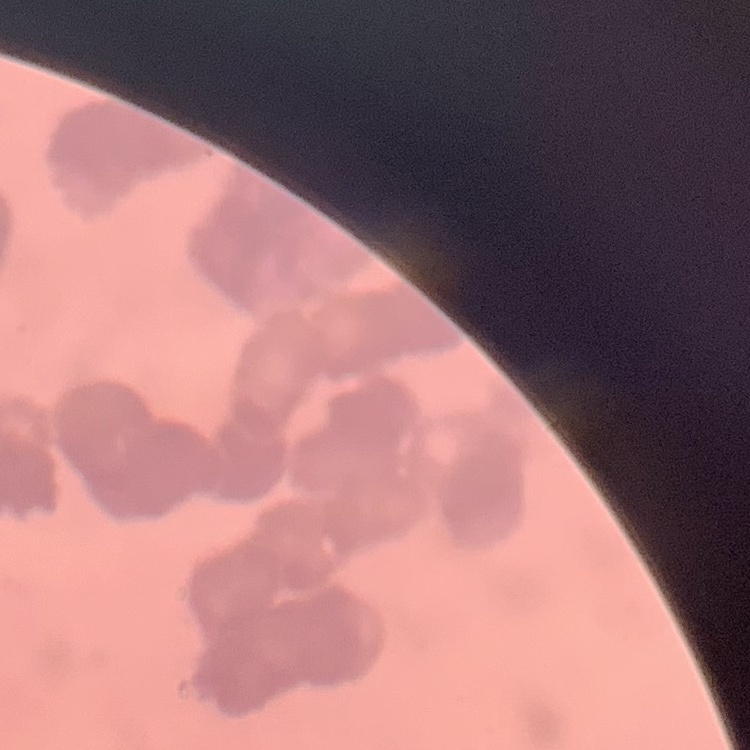

The erythrocytes exhibit rouleaux formation. Field's or Giemsa stain. Square crop of a larger photomicrograph. Thin blood film.